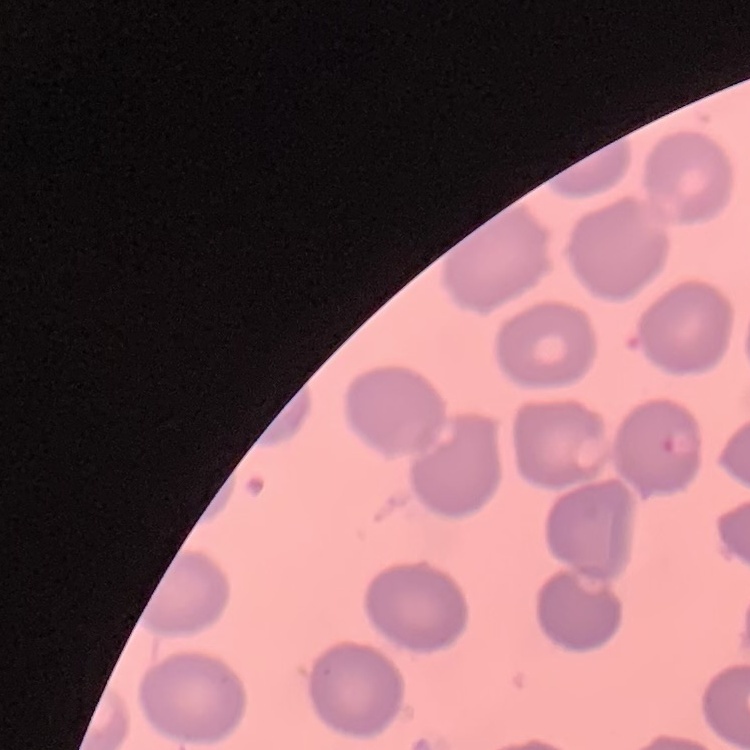
The erythrocytes show no rouleaux formation. Field's or Giemsa stain. One tile cut from a larger photomicrograph. Thin peripheral smear.